Report the malaria status of this cell.
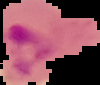

It is parasitized.

The area outside the segmented cell region is set to black. From a thin blood film. Image is 100×85 pixels.